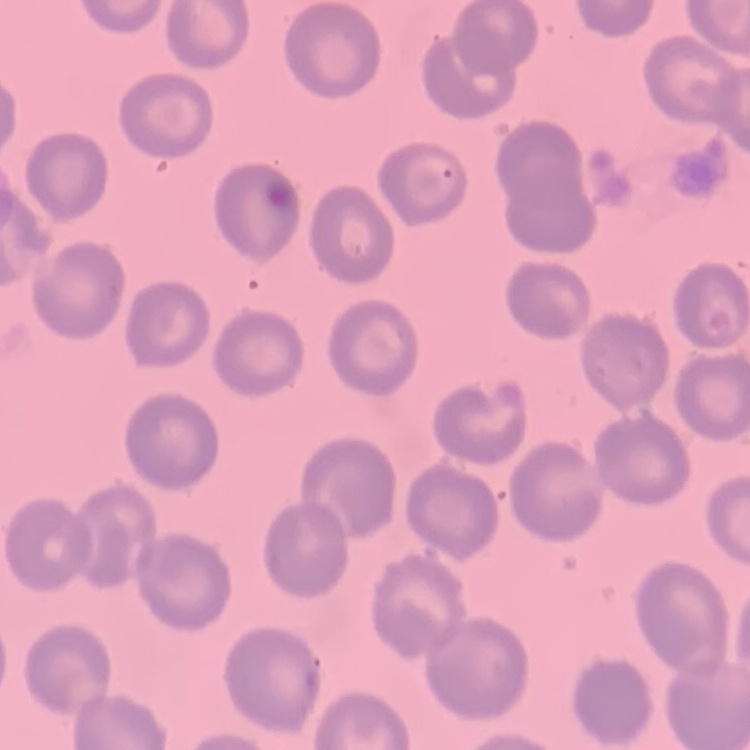
The erythrocytes show no rouleaux formation. Square crop of a larger photomicrograph. Thin blood smear. Stained with either Field's or Giemsa.